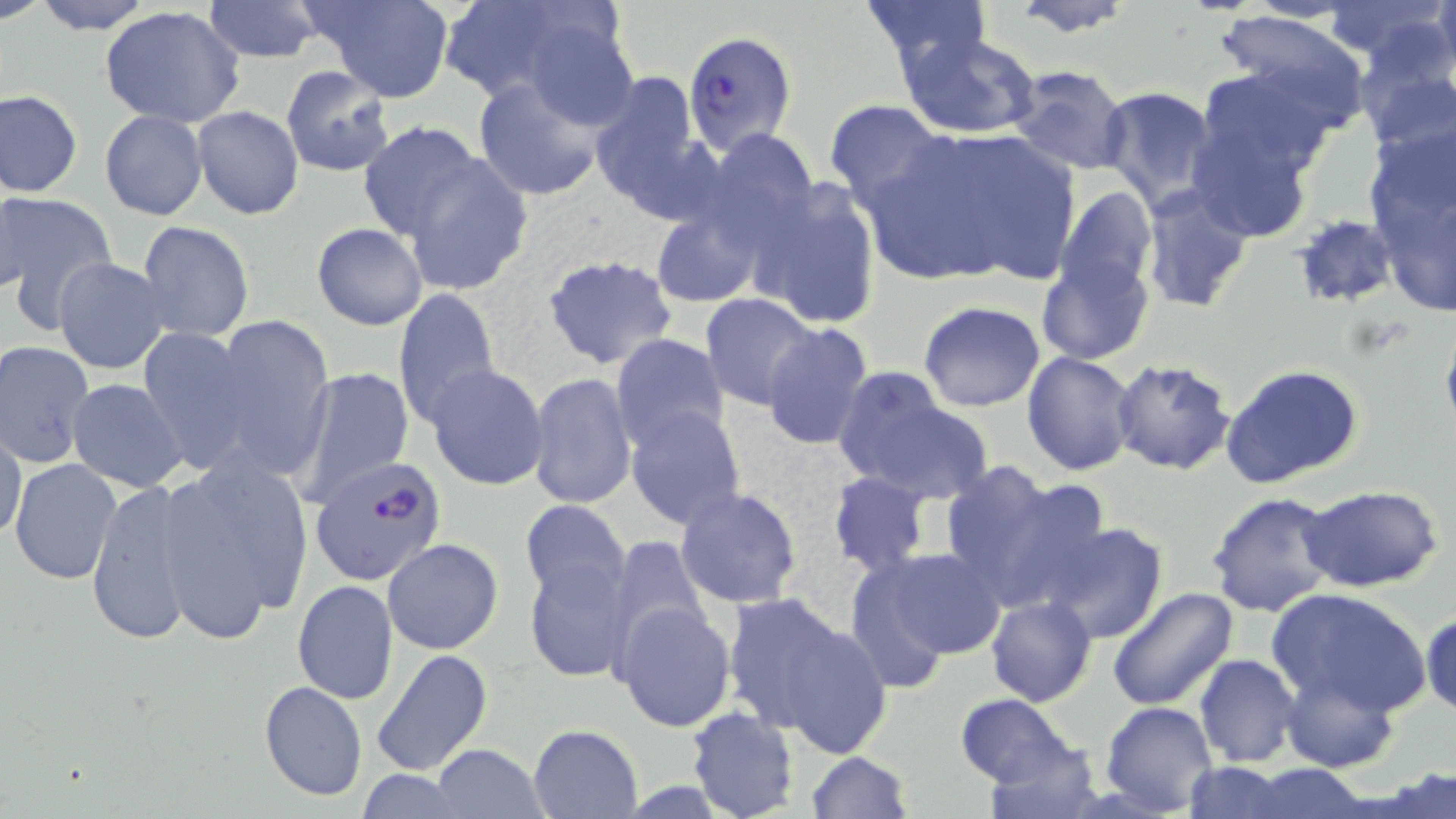
Summary:
  - Coordinate format: approximate bounding boxes as [x1, y1, x2, y2] in pixels
  - Uninfected red blood cell locations: [30, 0, 157, 36], [203, 0, 323, 64], [310, 0, 453, 103], [444, 0, 633, 119], [856, 0, 993, 72], [1011, 0, 1137, 37], [1236, 1, 1361, 25], [1322, 2, 1449, 63], [1431, 2, 1456, 80], [99, 6, 246, 130], [1213, 8, 1373, 132], [898, 30, 1040, 138], [1356, 43, 1456, 155], [1008, 64, 1132, 174], [281, 65, 395, 177], [1190, 69, 1339, 206], [588, 70, 708, 216], [472, 74, 608, 203], [1097, 85, 1219, 209], [1, 90, 83, 197], [824, 99, 948, 213], [193, 106, 305, 219], [98, 109, 208, 222], [357, 122, 485, 240], [877, 125, 1083, 288], [700, 128, 817, 246], [1365, 142, 1456, 318], [402, 154, 534, 299], [751, 180, 883, 331], [1140, 183, 1253, 312], [1055, 184, 1158, 306], [2, 186, 30, 296], [3, 193, 117, 320], [652, 208, 762, 306], [1293, 213, 1397, 307], [134, 220, 255, 342], [312, 223, 428, 330], [1036, 248, 1154, 367], [542, 252, 677, 371], [52, 256, 170, 374], [393, 287, 501, 425], [700, 292, 821, 411], [918, 301, 1045, 413], [208, 315, 334, 481], [759, 321, 873, 451], [138, 327, 259, 474], [610, 333, 730, 452], [0, 340, 96, 469], [1021, 352, 1138, 477], [1110, 360, 1237, 476], [425, 363, 550, 491], [1221, 363, 1364, 488], [297, 367, 415, 502], [830, 369, 990, 504], [526, 371, 637, 510], [67, 379, 189, 492], [624, 405, 747, 531], [1, 427, 26, 540], [146, 454, 316, 642], [9, 459, 123, 586], [940, 463, 1106, 615], [827, 471, 932, 577], [84, 478, 206, 648], [1299, 484, 1443, 593], [675, 485, 804, 608], [1207, 491, 1339, 617], [518, 499, 631, 606], [1039, 523, 1171, 644], [605, 536, 712, 652], [382, 537, 505, 655], [850, 547, 1006, 676], [522, 556, 636, 682], [292, 579, 399, 705], [1266, 586, 1431, 717], [1107, 589, 1240, 713], [723, 592, 880, 746], [985, 596, 1097, 707], [612, 601, 736, 732], [1420, 610, 1456, 718], [371, 647, 494, 776], [1194, 654, 1301, 767], [1282, 668, 1398, 771], [258, 681, 367, 802], [956, 693, 1075, 787], [1100, 702, 1218, 815], [685, 708, 798, 819], [528, 724, 644, 817], [981, 735, 1107, 818], [432, 743, 547, 818], [805, 751, 911, 819], [1183, 762, 1293, 818], [1243, 766, 1373, 818], [1378, 766, 1456, 818], [355, 769, 469, 819]
  - Plasmodium falciparum-infected red blood cell locations: [683, 31, 796, 156], [305, 461, 442, 589]
  - Slide-level diagnosis: Plasmodium falciparum
  - Modality: optical microscopy
  - Field of view: single
  - Preparation: thin blood smear
  - Magnification: 1000x
  - Stain: May-Grünwald-Giemsa
  - Image size: 1456×819 pixels